Give the position of every leukocyte visible.
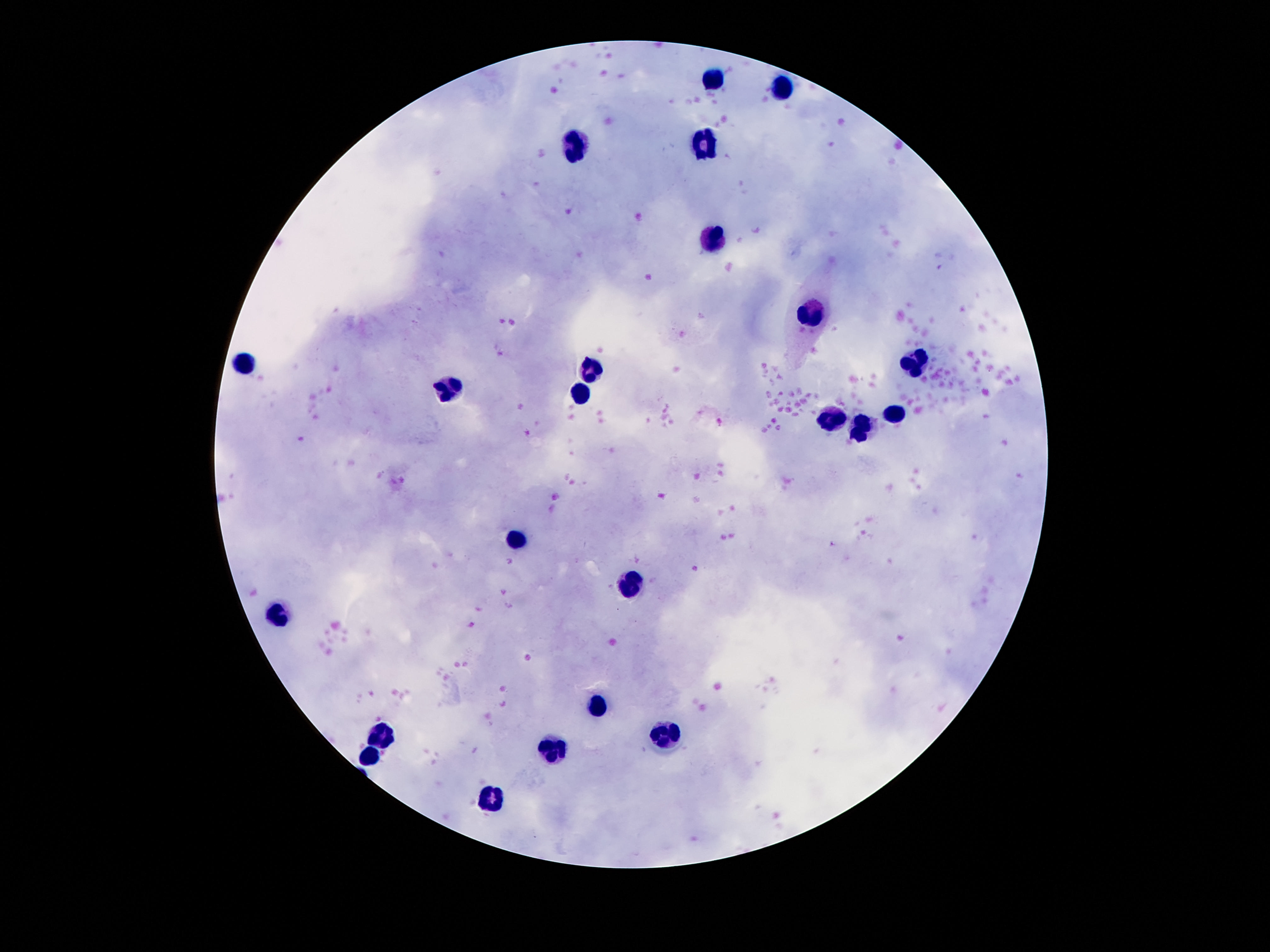

Approximate centers as (x, y) in pixels.
Leukocytes: (714, 76), (783, 88), (578, 143), (704, 143), (712, 238), (807, 316), (914, 363), (242, 364), (592, 370), (449, 387), (580, 391), (899, 411), (836, 421), (859, 431), (515, 540), (632, 584), (275, 615), (597, 705), (662, 731), (382, 735), (559, 747), (368, 760), (489, 802).

{
  "image_size": "1270×952 pixels",
  "magnification": "100x",
  "field_of_view": "one from this slide",
  "capture": "smartphone camera through the microscope eyepiece",
  "stain": "Giemsa",
  "patient_malaria_status": "uninfected",
  "preparation": "thick blood film"
}